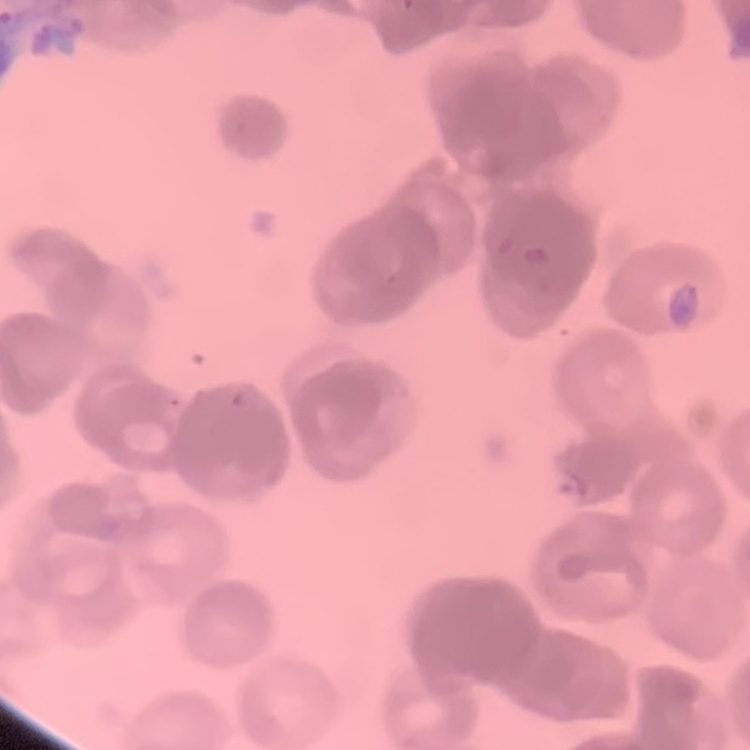
The erythrocytes exhibit rouleaux formation. Thin peripheral smear. One tile cut from a larger photomicrograph. Stained with either Field's or Giemsa.